Classify this cell by malaria status.
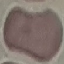
It is uninfected.

Thin smear of blood. Photographed with a smartphone camera at the microscope eyepiece. Giemsa stain. Cell patch, automatically extracted from a larger field of view and resized to 64 × 64 pixels.